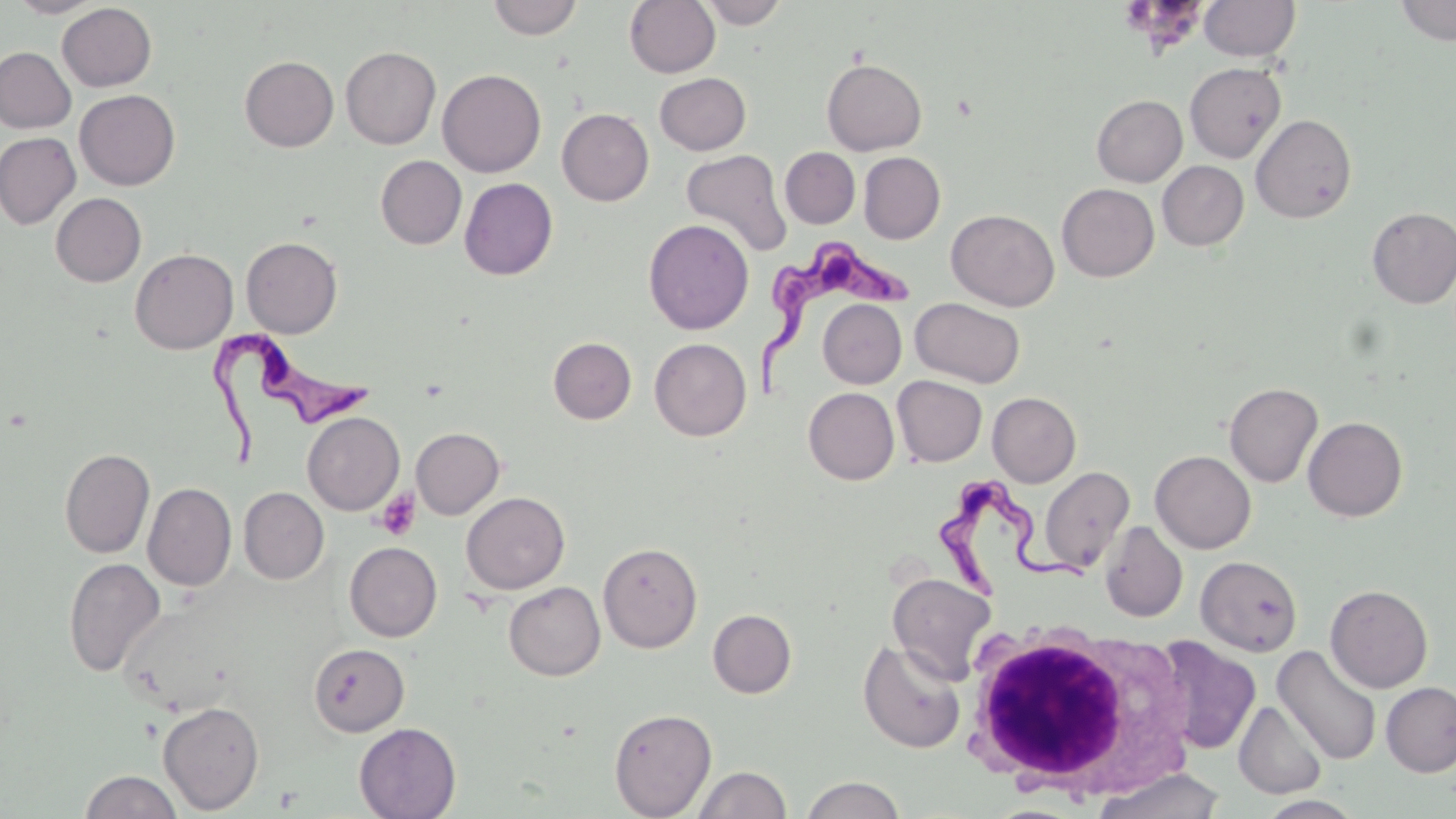

Summary:
  - Coordinate format: approximate bounding boxes as [x1, y1, x2, y2] in pixels
  - Platelet locations: [375, 488, 421, 540]
  - Trypanosoma brucei locations: [759, 237, 921, 399], [208, 326, 382, 475], [929, 477, 1086, 600]
  - Uninfected red blood cell locations: [7, 0, 105, 18], [487, 0, 583, 40], [624, 0, 720, 77], [697, 0, 790, 28], [1200, 0, 1300, 61], [1395, 0, 1456, 45], [57, 3, 156, 91], [341, 46, 441, 149], [1, 47, 75, 133], [239, 56, 339, 151], [822, 58, 927, 155], [1184, 62, 1287, 163], [437, 68, 546, 177], [655, 72, 751, 155], [74, 89, 180, 190], [1092, 95, 1187, 186], [557, 108, 654, 206], [1251, 114, 1357, 223], [0, 132, 80, 230], [780, 147, 860, 228], [680, 149, 792, 257], [859, 152, 945, 243], [375, 155, 467, 249], [1157, 160, 1249, 251], [459, 178, 558, 280], [1057, 183, 1159, 281], [51, 193, 146, 286], [1367, 207, 1456, 308], [946, 209, 1060, 311], [643, 219, 754, 335], [241, 236, 343, 338], [130, 248, 238, 354], [910, 297, 1025, 387], [818, 299, 906, 388], [548, 337, 636, 424], [650, 338, 751, 441], [892, 375, 987, 466], [1224, 382, 1323, 487], [803, 387, 899, 484], [987, 392, 1081, 487], [302, 412, 405, 515], [1303, 416, 1408, 522], [411, 427, 504, 519], [59, 448, 155, 558], [1150, 450, 1256, 554], [1038, 466, 1134, 573], [143, 482, 236, 591], [239, 487, 329, 584], [461, 492, 570, 594], [1101, 522, 1188, 622], [344, 541, 442, 642], [598, 542, 703, 653], [1196, 556, 1303, 656], [63, 557, 166, 677], [887, 571, 998, 684], [504, 581, 605, 680], [1325, 585, 1433, 693], [708, 609, 797, 698], [1153, 637, 1261, 755], [858, 639, 966, 753], [308, 643, 409, 736], [1273, 645, 1382, 766], [1381, 681, 1456, 777], [1234, 700, 1328, 800], [157, 701, 265, 814], [608, 708, 716, 818], [354, 722, 461, 819], [692, 765, 791, 819], [80, 769, 182, 819], [1091, 769, 1227, 819], [800, 775, 906, 819]
  - White blood cell locations: [956, 621, 1194, 802]
  - Slide-level diagnosis: Trypanosoma brucei
  - Image size: 1456×819 pixels
  - Field of view: single
  - Stain: May-Grünwald-Giemsa
  - Preparation: thin blood film
  - Modality: light microscopy
  - Magnification: 1000x